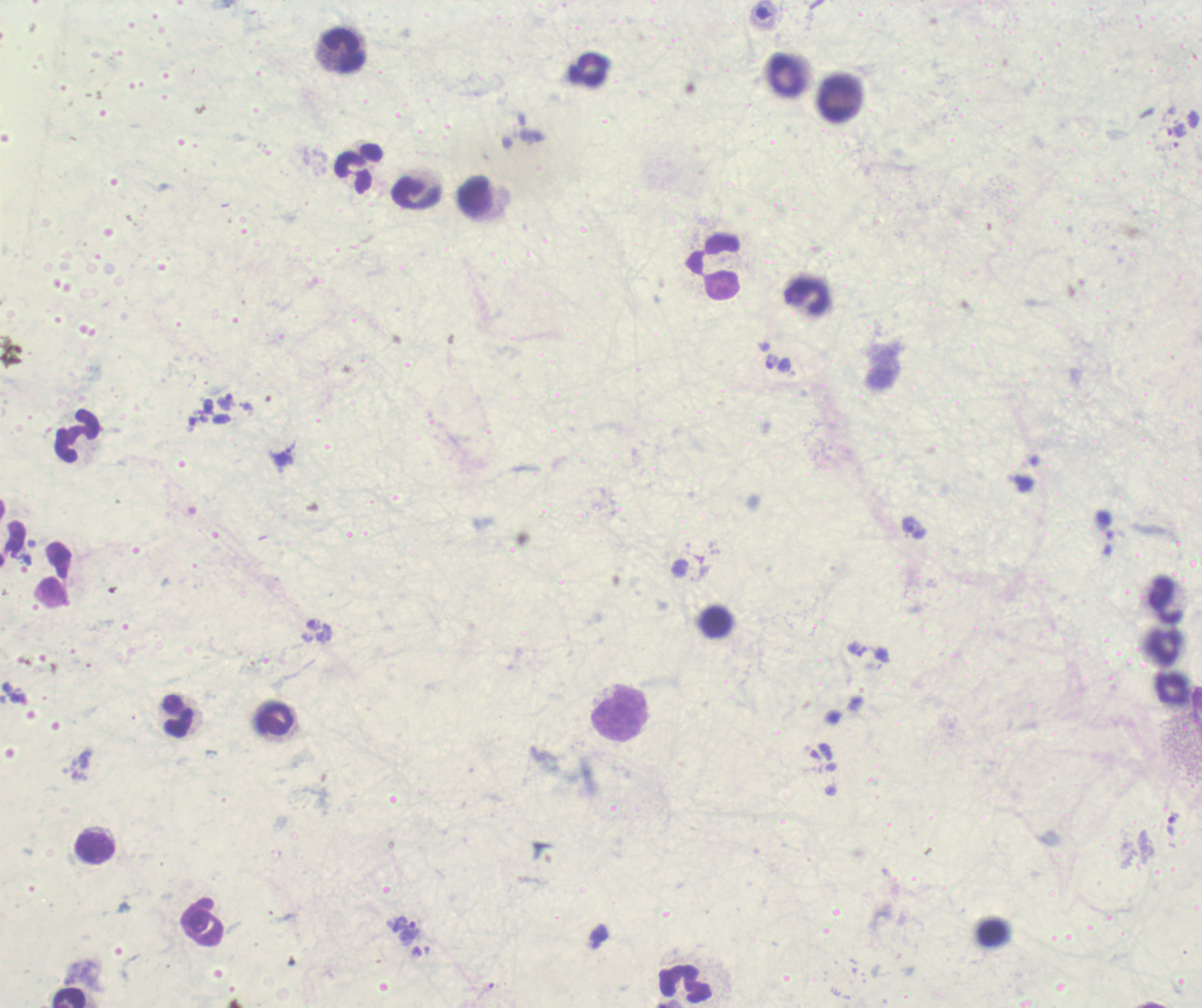

magnification: 100x
context: previously used in an actual diagnosis
image_size: 1202×1008 pixels
leukocyte_locations: 'approximate centers as [x, y] in pixels: [343, 50], [590, 68], [786, 75], [840, 97], [358, 168], [416, 193], [475, 196], [713, 266], [807, 296], [77, 435], [54, 575], [1166, 600], [716, 623], [1166, 647], [1171, 688], [619, 714], [178, 716], [273, 718], [96, 847], [201, 922], [992, 934], [684, 983], [68, 996]'
field_of_view: single
result: Plasmodium parasites detected
trophozoite_locations: 'approximate centers as [x, y] in pixels: [855, 649], [876, 654], [404, 930]'
preparation: thick smear of blood
coloration_quality: bad
background_quality: poor
stain: Romanowsky